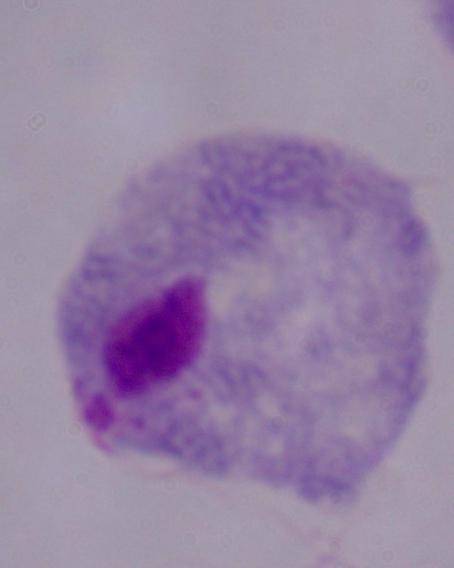

Photomicrograph. A trichomonad is shown. 1000x magnification.